Assess the morphology of the red blood cells.
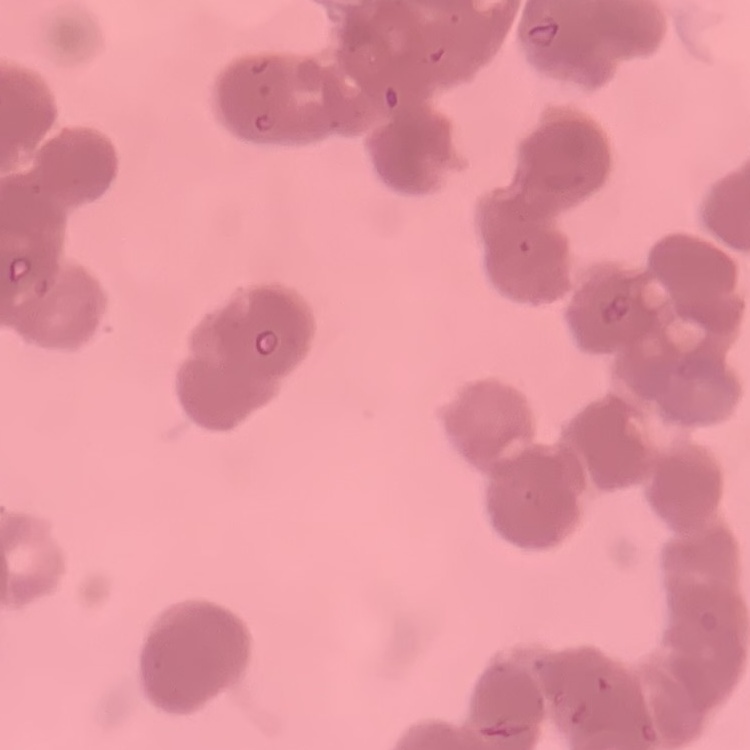

Rouleaux formation.

{
  "preparation": "thin blood film",
  "stain": "Field's or Giemsa",
  "image_type": "square crop of a larger photomicrograph"
}